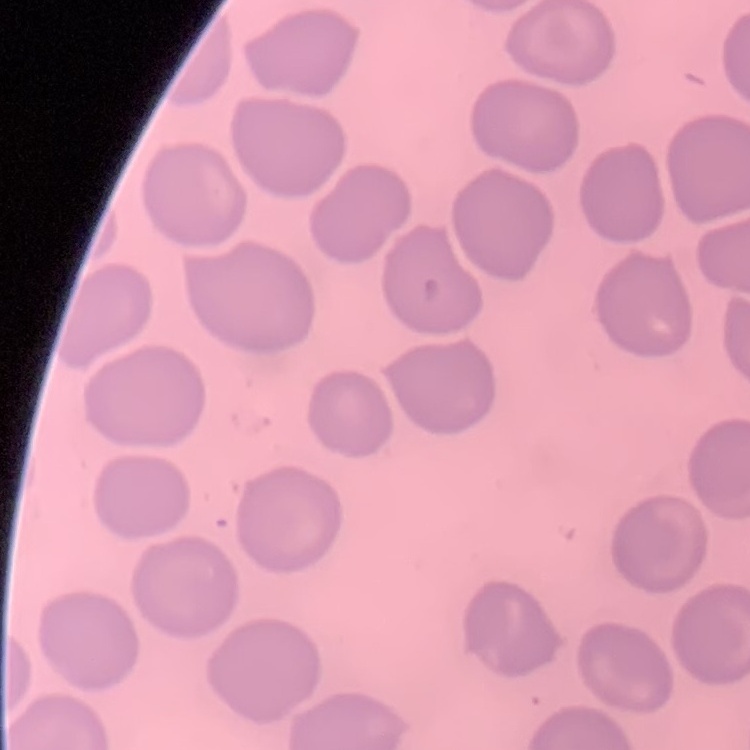
erythrocyte morphology = no rouleaux formation
preparation = thin peripheral smear
image type = one tile cut from a larger photomicrograph
stain = Field's or Giemsa